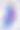

Summary:
  - Magnification: 400x
  - Identification: Toxoplasma gondii
  - Modality: photomicrograph